State the blood parasite species.
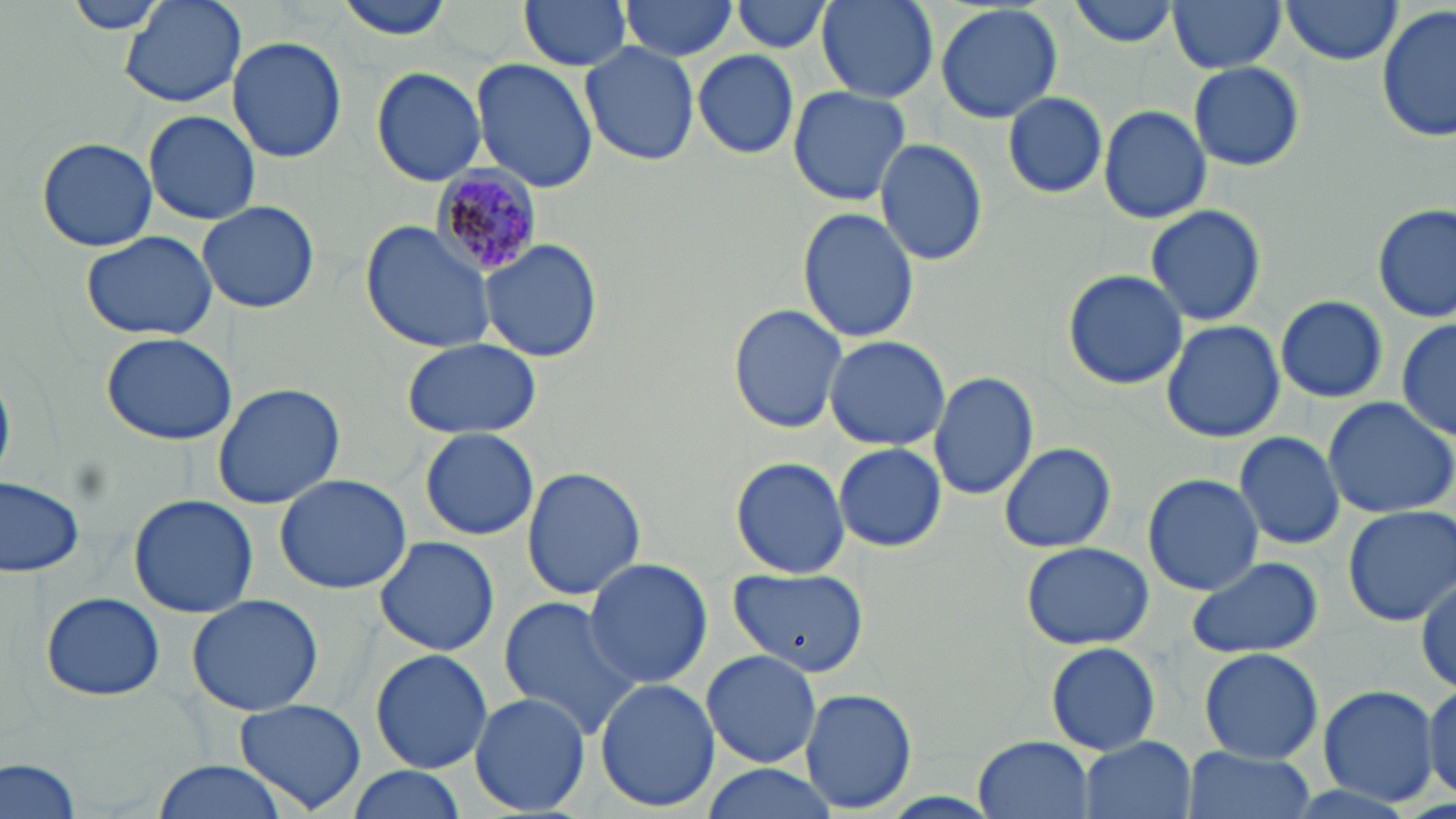
Plasmodium malariae.

Summary:
  - Coordinate format: approximate bounding boxes as (x1, y1, x2, y2) in pixels
  - Uninfected red blood cell locations: (119, 0, 248, 108), (332, 0, 460, 41), (517, 0, 633, 71), (617, 0, 738, 61), (729, 0, 835, 54), (815, 0, 939, 104), (1070, 0, 1180, 48), (1167, 0, 1286, 74), (1278, 0, 1405, 66), (63, 1, 178, 36), (935, 4, 1064, 123), (1378, 6, 1455, 145), (227, 35, 347, 164), (580, 42, 701, 166), (693, 50, 800, 160), (472, 60, 598, 193), (1188, 61, 1305, 172), (370, 66, 487, 187), (787, 85, 912, 206), (1003, 90, 1107, 199), (1098, 104, 1212, 224), (143, 110, 260, 225), (37, 137, 157, 251), (874, 137, 989, 267), (198, 199, 320, 314), (1143, 203, 1267, 327), (1373, 204, 1453, 324), (797, 207, 920, 346), (359, 219, 500, 355), (80, 230, 218, 342), (479, 239, 604, 362), (1062, 268, 1188, 390), (1276, 294, 1389, 403), (728, 304, 846, 433), (1395, 317, 1455, 440), (1161, 320, 1284, 443), (101, 331, 237, 446), (822, 335, 951, 451), (402, 337, 542, 440), (927, 369, 1039, 502), (212, 383, 345, 508), (1320, 396, 1456, 519), (419, 427, 539, 541), (1233, 430, 1348, 549), (998, 440, 1117, 553), (833, 442, 947, 553), (729, 456, 850, 578), (521, 465, 646, 600), (274, 473, 411, 595), (1142, 473, 1265, 595), (0, 477, 84, 578), (127, 494, 258, 617), (1342, 505, 1456, 626), (372, 537, 501, 656), (1020, 540, 1156, 650), (1186, 554, 1322, 661), (583, 557, 713, 689), (726, 567, 869, 676), (1414, 576, 1455, 698), (41, 591, 166, 703), (186, 594, 325, 717), (498, 597, 640, 737), (1045, 641, 1162, 755), (1199, 647, 1323, 763), (369, 648, 493, 773), (700, 648, 822, 768), (594, 676, 720, 812), (1424, 681, 1456, 804), (1317, 685, 1440, 809), (799, 687, 918, 812), (469, 691, 591, 815), (232, 698, 368, 816), (973, 735, 1097, 818), (1078, 735, 1197, 819), (1182, 749, 1316, 819), (0, 755, 83, 819), (148, 759, 294, 819), (698, 764, 839, 819), (344, 766, 469, 819)
  - Plasmodium malariae-infected red blood cell locations: (430, 169, 541, 276)
  - Image size: 1456×819 pixels
  - Modality: optical microscopy
  - Stain: May-Grünwald-Giemsa
  - Field of view: one of a larger specimen
  - Magnification: 1000x
  - Preparation: thin blood film